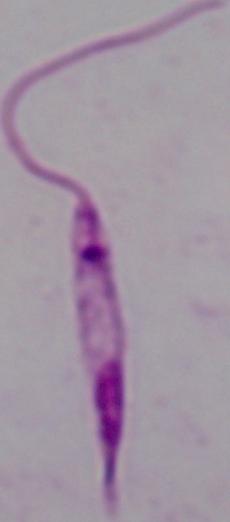

Micrograph. A Leishmania parasite is shown. Captured at 1000x magnification.